Report the malaria status of this cell.
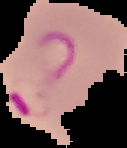

It is parasitized.

{
  "image_type": "segmented cell region on a black background",
  "preparation": "thin blood smear",
  "image_size": "127×148 pixels"
}